Identify the blood parasite species.
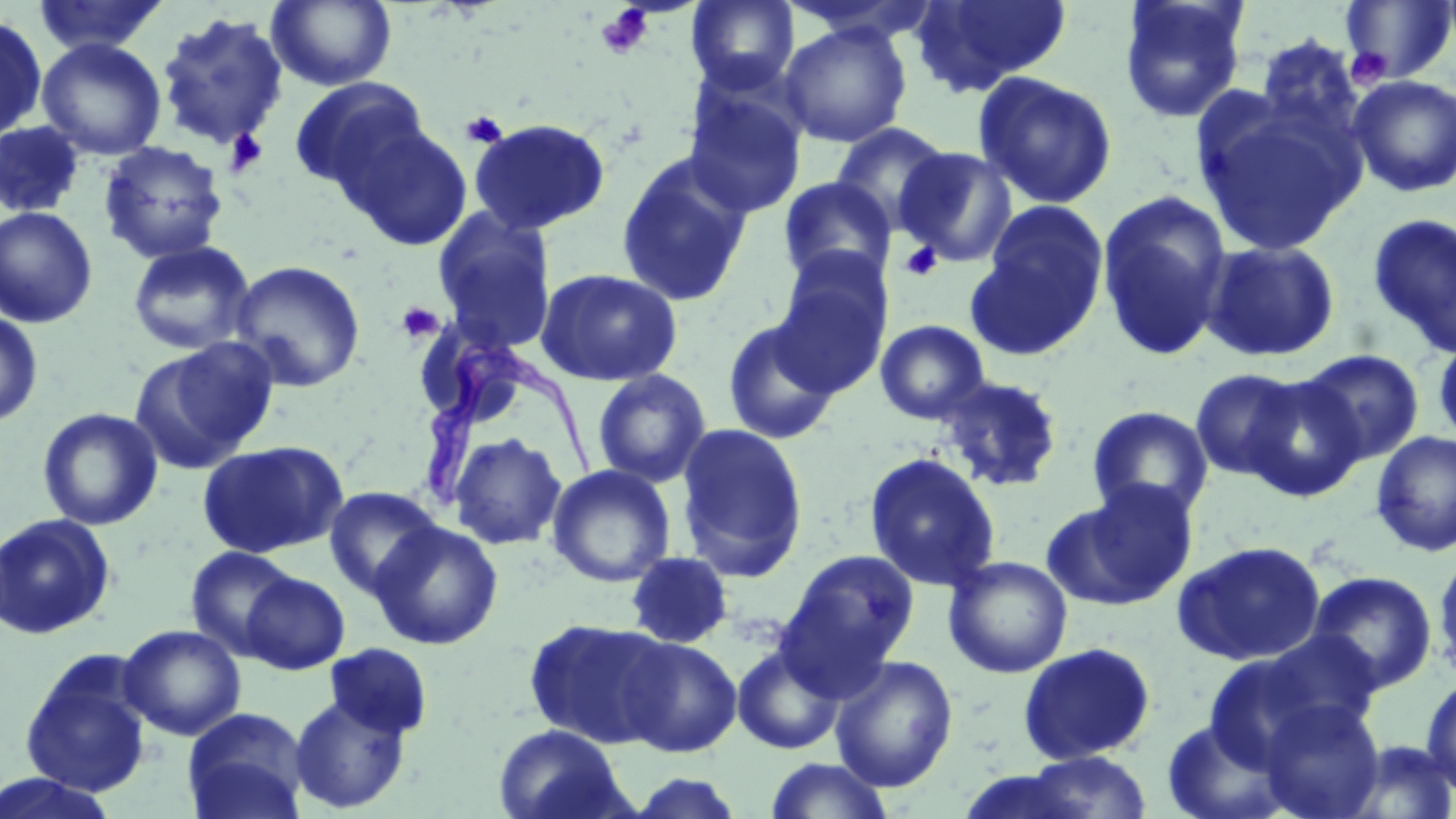

Trypanosoma brucei.

Approximate bounding boxes as named x1/y1/x2/y2 corners in pixels. Uninfected red blood cell locations: (x1=31, y1=0, x2=169, y2=56), (x1=267, y1=0, x2=397, y2=91), (x1=685, y1=0, x2=801, y2=94), (x1=776, y1=0, x2=943, y2=46), (x1=911, y1=0, x2=1072, y2=95), (x1=1118, y1=0, x2=1251, y2=123), (x1=1437, y1=0, x2=1456, y2=53), (x1=1340, y1=1, x2=1456, y2=84), (x1=156, y1=11, x2=289, y2=151), (x1=0, y1=16, x2=47, y2=142), (x1=778, y1=23, x2=912, y2=147), (x1=1252, y1=34, x2=1365, y2=136), (x1=37, y1=39, x2=167, y2=160), (x1=973, y1=71, x2=1118, y2=209), (x1=1348, y1=75, x2=1456, y2=197), (x1=289, y1=77, x2=431, y2=198), (x1=682, y1=85, x2=808, y2=219), (x1=1197, y1=102, x2=1358, y2=254), (x1=467, y1=117, x2=611, y2=236), (x1=340, y1=119, x2=474, y2=252), (x1=0, y1=121, x2=85, y2=217), (x1=830, y1=122, x2=953, y2=233), (x1=97, y1=141, x2=228, y2=264), (x1=895, y1=147, x2=1017, y2=267), (x1=615, y1=152, x2=755, y2=307), (x1=778, y1=177, x2=896, y2=287), (x1=1096, y1=190, x2=1233, y2=362), (x1=972, y1=200, x2=1110, y2=354), (x1=0, y1=206, x2=99, y2=329), (x1=432, y1=210, x2=558, y2=354), (x1=1366, y1=212, x2=1456, y2=358), (x1=1201, y1=239, x2=1341, y2=363), (x1=127, y1=240, x2=255, y2=357), (x1=772, y1=256, x2=894, y2=394), (x1=228, y1=259, x2=366, y2=392), (x1=536, y1=268, x2=684, y2=387), (x1=0, y1=310, x2=43, y2=428), (x1=721, y1=317, x2=842, y2=446), (x1=874, y1=319, x2=991, y2=424), (x1=1433, y1=336, x2=1456, y2=450), (x1=132, y1=339, x2=280, y2=473), (x1=1298, y1=348, x2=1425, y2=465), (x1=1189, y1=368, x2=1307, y2=482), (x1=592, y1=369, x2=711, y2=488), (x1=937, y1=374, x2=1065, y2=493), (x1=1240, y1=375, x2=1366, y2=501), (x1=1086, y1=405, x2=1214, y2=521), (x1=37, y1=407, x2=163, y2=531), (x1=675, y1=422, x2=809, y2=582), (x1=1371, y1=430, x2=1456, y2=557), (x1=448, y1=432, x2=567, y2=550), (x1=197, y1=440, x2=348, y2=559), (x1=864, y1=453, x2=1000, y2=592), (x1=547, y1=464, x2=676, y2=587), (x1=1064, y1=479, x2=1200, y2=607), (x1=323, y1=486, x2=443, y2=599), (x1=0, y1=513, x2=116, y2=640), (x1=369, y1=520, x2=505, y2=650), (x1=1171, y1=540, x2=1327, y2=667), (x1=185, y1=546, x2=299, y2=658), (x1=777, y1=549, x2=920, y2=685), (x1=625, y1=550, x2=734, y2=650), (x1=1433, y1=550, x2=1456, y2=683), (x1=943, y1=555, x2=1073, y2=678), (x1=1306, y1=570, x2=1438, y2=693), (x1=241, y1=571, x2=350, y2=675), (x1=523, y1=617, x2=675, y2=749), (x1=118, y1=624, x2=246, y2=740), (x1=618, y1=636, x2=742, y2=757), (x1=1204, y1=636, x2=1375, y2=763), (x1=1017, y1=642, x2=1157, y2=765), (x1=323, y1=643, x2=434, y2=740), (x1=731, y1=643, x2=846, y2=755), (x1=18, y1=654, x2=154, y2=798), (x1=830, y1=656, x2=958, y2=791), (x1=1421, y1=674, x2=1456, y2=798), (x1=288, y1=692, x2=412, y2=814), (x1=1256, y1=699, x2=1386, y2=819), (x1=181, y1=707, x2=309, y2=819), (x1=1160, y1=718, x2=1294, y2=819), (x1=492, y1=723, x2=634, y2=819), (x1=1339, y1=739, x2=1456, y2=818), (x1=1010, y1=751, x2=1156, y2=819), (x1=764, y1=758, x2=896, y2=819), (x1=0, y1=771, x2=124, y2=818), (x1=623, y1=771, x2=747, y2=818). Trypanosoma brucei locations: (x1=412, y1=338, x2=601, y2=514). Platelet locations: (x1=595, y1=4, x2=655, y2=60), (x1=1344, y1=46, x2=1393, y2=88), (x1=460, y1=110, x2=508, y2=149), (x1=223, y1=129, x2=269, y2=178), (x1=899, y1=240, x2=943, y2=282), (x1=396, y1=302, x2=445, y2=344). Optical microscopy. May-Grünwald-Giemsa-stained preparation. Image is 1456×819 pixels. One field of a larger specimen. 1000x magnification. Thin blood film.